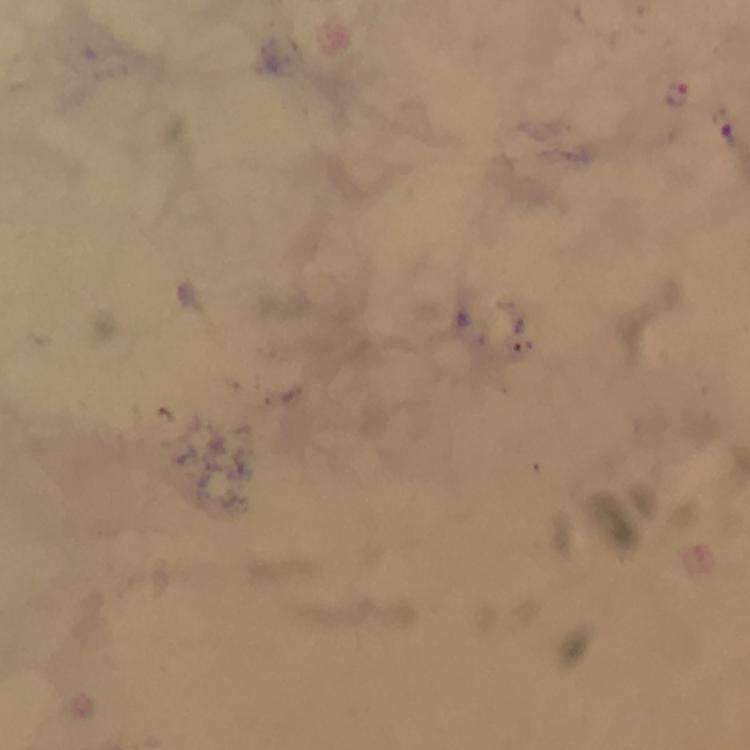

immersion oil = applied
capture = smartphone mounted on the microscope
magnification = 100x
cropped from = one field of view
image size = 750×750 pixels
stain = Giemsa
preparation = thick blood smear
malaria parasite locations = approximate object centers, in pixels from the top-left corner: (x=677, y=96), (x=728, y=131)
context = from a diagnostic examination for malaria